Give the extent of all white blood cells.
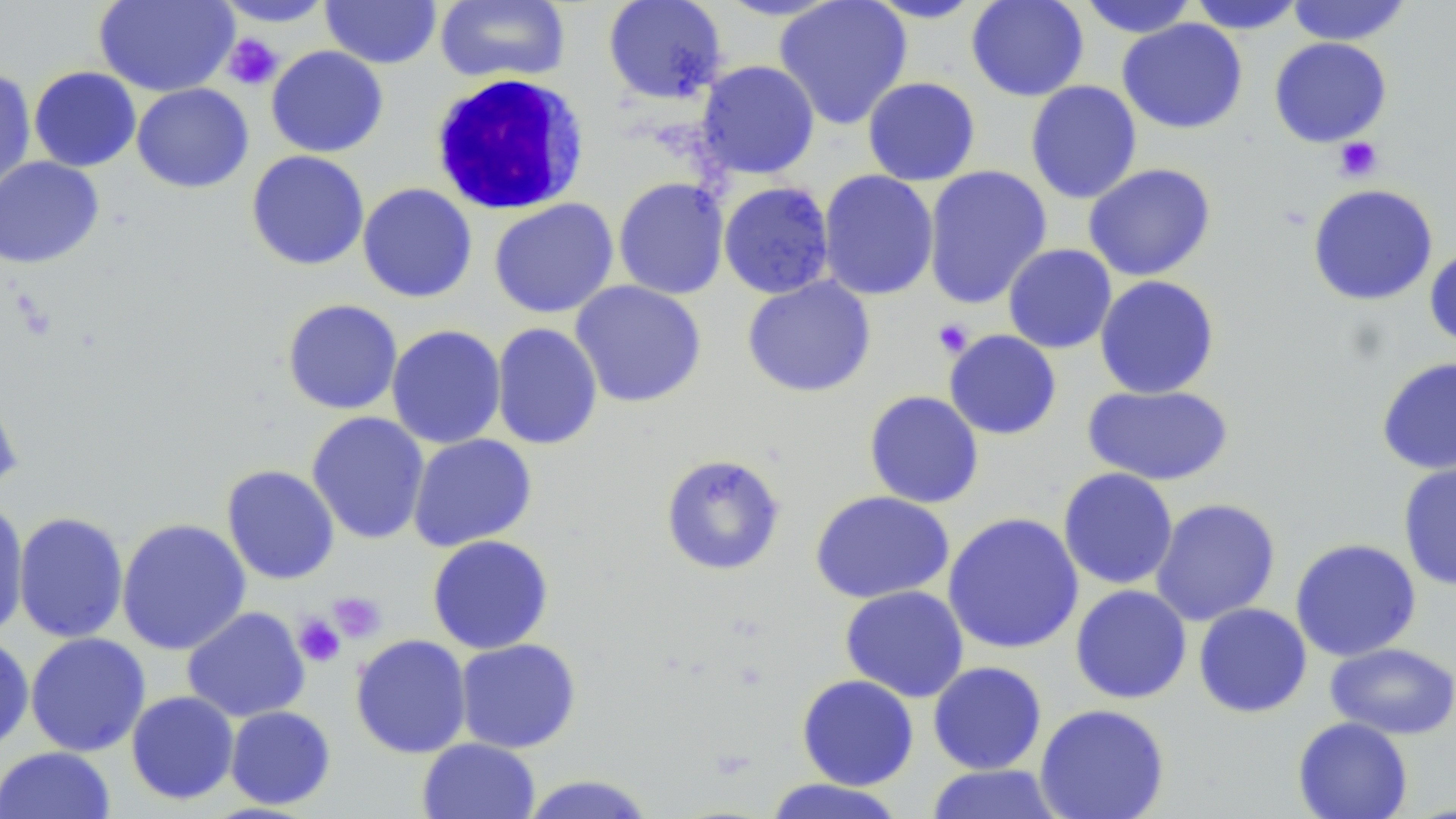

Approximate bounding boxes as [x1, y1, x2, y2] in pixels.
White blood cells: [429, 73, 590, 216].

Platelet locations: [222, 33, 284, 90], [1333, 137, 1382, 182], [932, 318, 974, 358], [328, 591, 386, 643], [293, 613, 345, 667]. Uninfected red blood cell locations: [94, 0, 238, 97], [213, 0, 338, 27], [434, 0, 571, 85], [602, 0, 727, 104], [773, 0, 913, 129], [862, 0, 987, 23], [966, 0, 1089, 102], [1077, 0, 1199, 38], [1285, 0, 1413, 46], [320, 1, 442, 69], [1186, 1, 1307, 34], [1117, 18, 1248, 134], [1269, 37, 1392, 147], [265, 45, 389, 157], [696, 60, 820, 179], [28, 66, 141, 172], [0, 68, 36, 197], [862, 76, 981, 186], [1025, 80, 1142, 204], [131, 83, 254, 193], [246, 150, 370, 271], [0, 156, 105, 269], [1082, 162, 1216, 282], [922, 165, 1052, 310], [817, 170, 939, 301], [613, 177, 730, 300], [718, 181, 835, 299], [357, 183, 478, 303], [1307, 183, 1438, 306], [488, 198, 618, 318], [1003, 243, 1117, 354], [1424, 246, 1456, 352], [1094, 275, 1220, 399], [741, 276, 876, 398], [570, 280, 707, 408], [281, 299, 403, 415], [491, 322, 603, 451], [386, 324, 506, 449], [944, 330, 1062, 440], [1376, 356, 1456, 474], [0, 377, 23, 499], [1082, 384, 1234, 486], [864, 390, 984, 509], [306, 412, 430, 544], [407, 433, 537, 552], [659, 453, 786, 576], [1397, 459, 1456, 592], [221, 464, 340, 585], [1058, 468, 1179, 590], [810, 490, 955, 603], [1150, 497, 1281, 626], [0, 499, 29, 640], [13, 511, 129, 644], [942, 512, 1084, 654], [116, 517, 252, 655], [427, 534, 554, 654], [1289, 538, 1422, 662], [840, 585, 969, 703], [1070, 585, 1192, 704], [1193, 602, 1312, 718], [182, 606, 310, 722], [25, 632, 151, 757], [0, 633, 34, 755], [350, 634, 472, 759], [455, 638, 581, 754], [1325, 642, 1456, 739], [927, 661, 1047, 775], [796, 674, 919, 791], [126, 690, 240, 805], [1034, 703, 1170, 819], [224, 705, 336, 810], [1292, 716, 1413, 819], [417, 737, 541, 819], [0, 746, 116, 819], [924, 764, 1064, 819], [519, 774, 657, 818], [761, 778, 909, 818]. Slide-level diagnosis: no evidence of blood parasites. Optical microscopy. May-Grünwald-Giemsa-stained preparation. Single field of view. 1000x magnification. Image is 1456×819 pixels. Thin blood film.